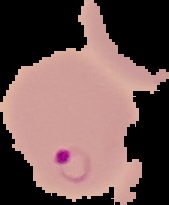

Malaria status: parasitized. The area outside the segmented cell region is set to black. Image is 169×205 pixels. From a thin blood smear.